Evaluate for malaria.
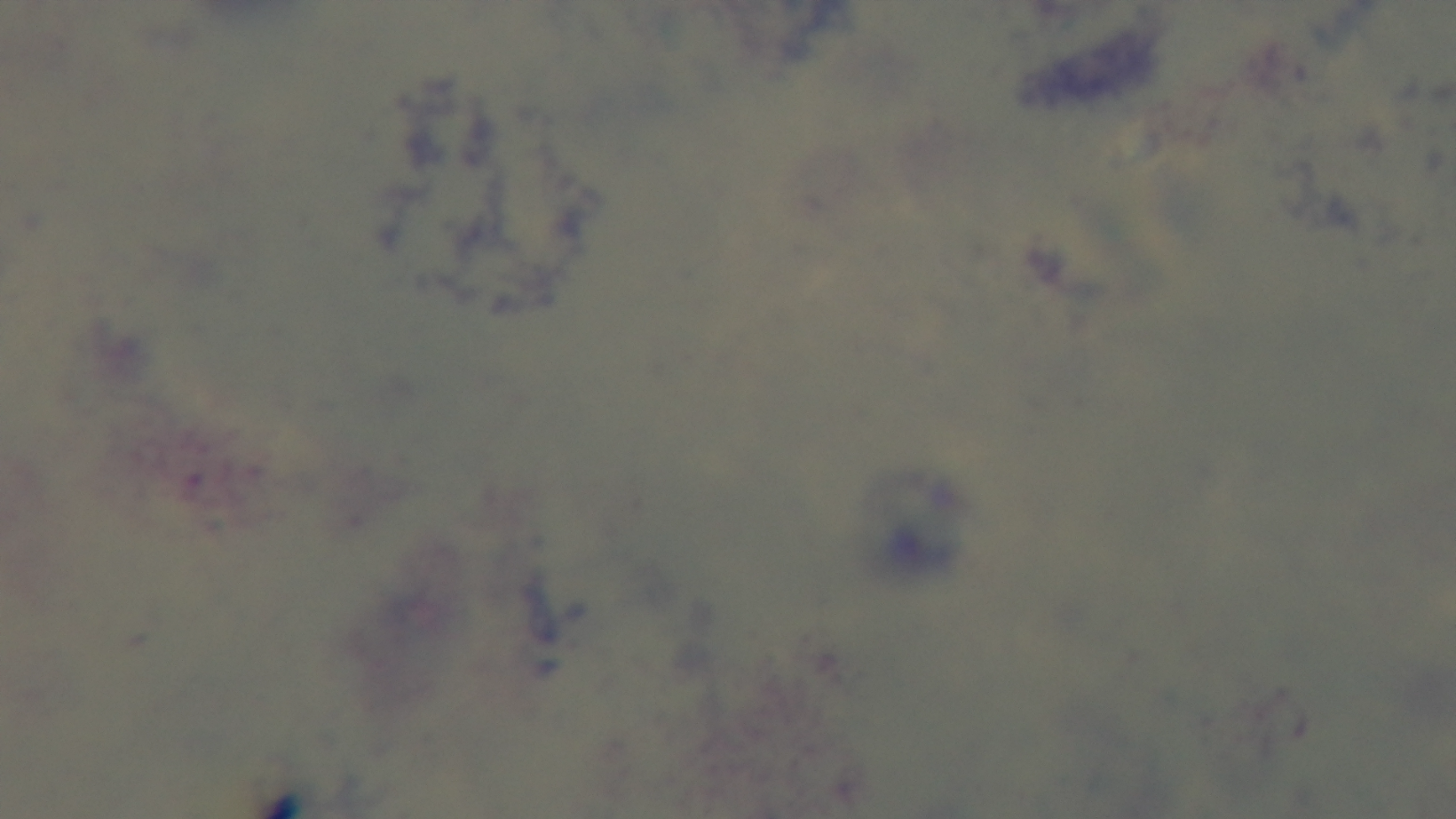

Uninfected.

Summary:
  - Field of view: one from the slide
  - Objective: 100x oil immersion
  - Modality: light microscopy
  - Preparation: thick
  - Stain: Giemsa
  - Capture: mounted 4K digital camera